Describe the morphology of the red blood cells.
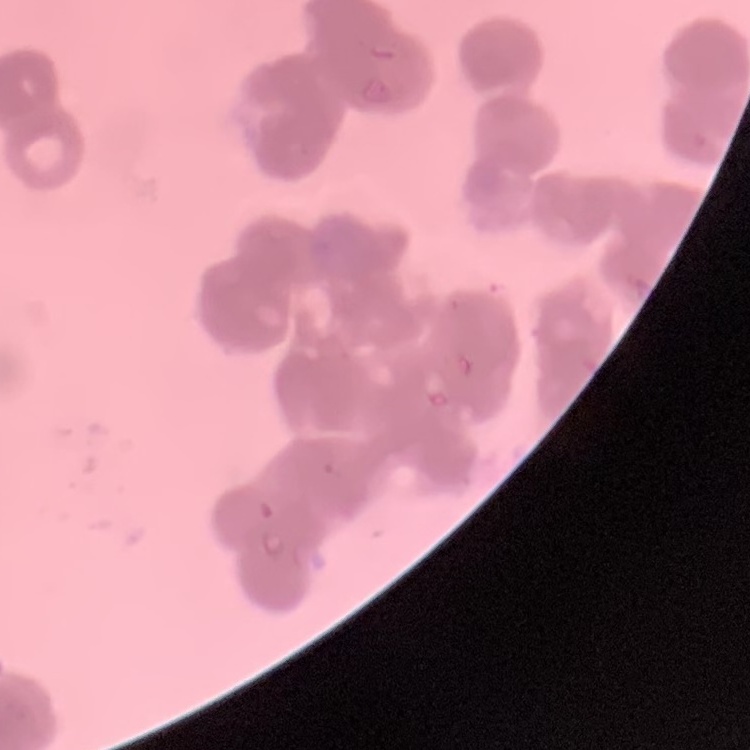

Rouleaux formation.

stain = Field's or Giemsa
image type = one tile cut from a larger photomicrograph
preparation = thin blood film